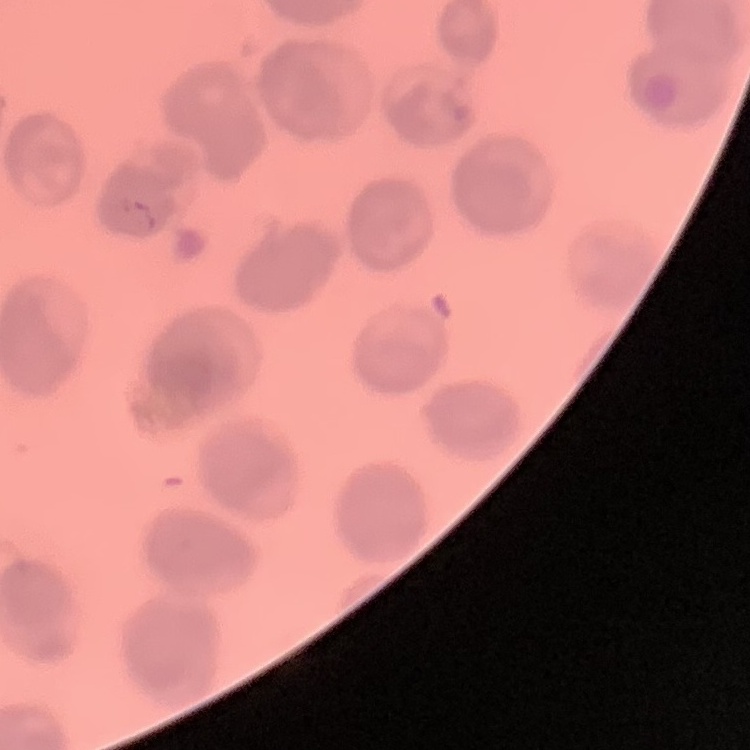 The erythrocytes show no rouleaux formation. Thin peripheral smear. Stained with either Field's or Giemsa. Square crop of a larger photomicrograph.